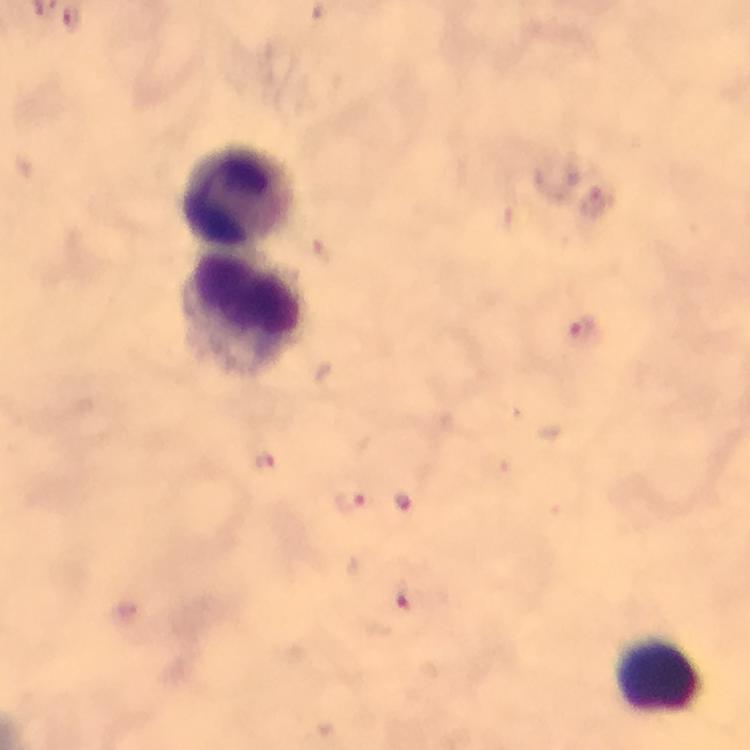 Approximate centers as {x, y} in pixels. Leukocyte locations: {239, 195}, {244, 314}, {662, 678}. Malaria parasite locations: {597, 203}, {581, 331}, {266, 462}, {350, 501}, {405, 501}, {405, 597}. Thick blood film. Cropped region of a single field of view. From a diagnostic examination for malaria. Immersion oil was used. Image is 750×750 pixels. Giemsa stain. At 100x magnification. Smartphone photograph taken through a microscope.